Locate every blood parasite and identify its species.
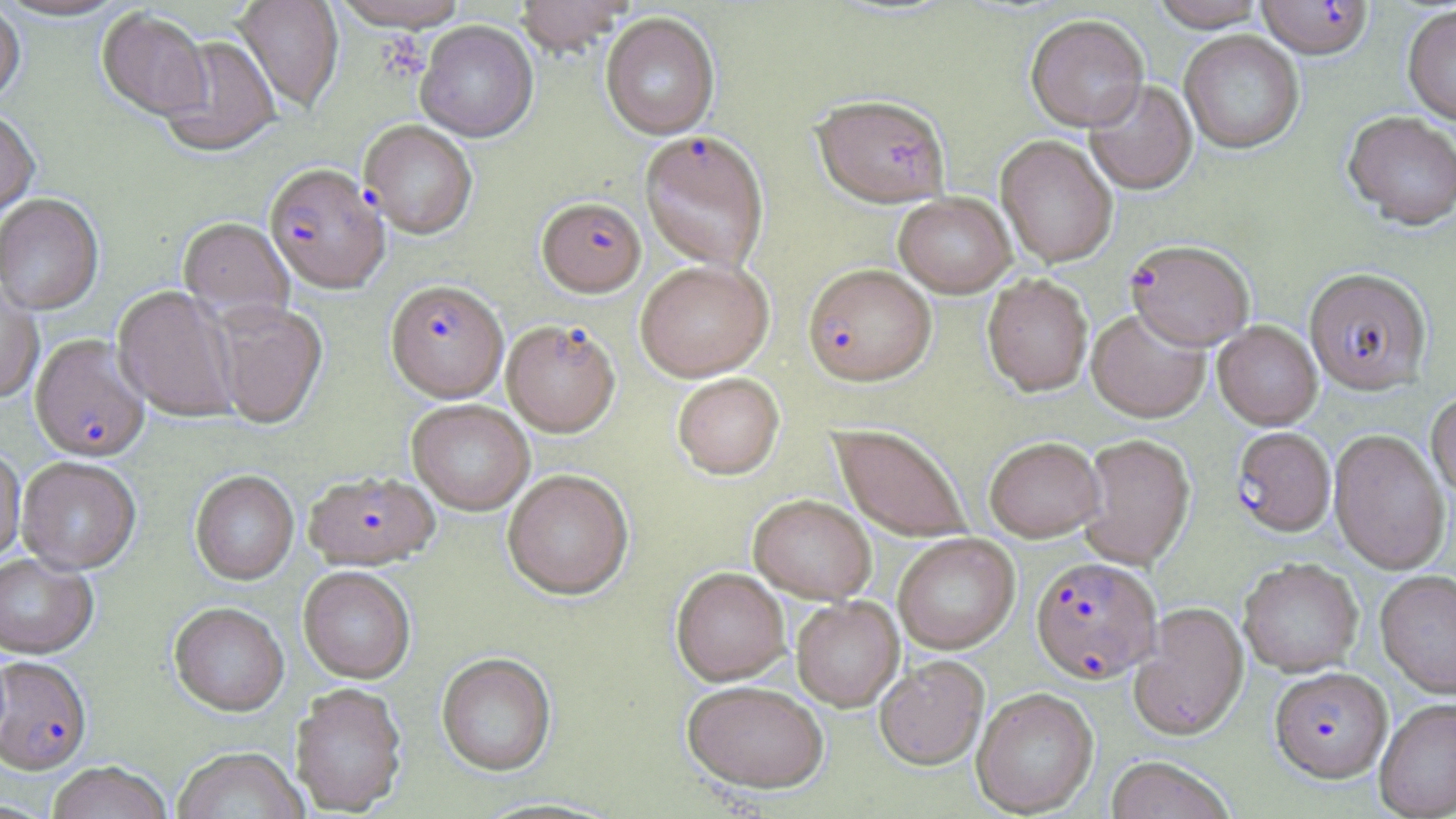

Approximate bounding boxes as named x1/y1/x2/y2 corners in pixels.
Plasmodium falciparum-infected red blood cells: (x1=1256, y1=0, x2=1374, y2=59), (x1=359, y1=121, x2=477, y2=239), (x1=639, y1=130, x2=770, y2=271), (x1=264, y1=164, x2=390, y2=295), (x1=537, y1=196, x2=646, y2=296), (x1=1126, y1=239, x2=1255, y2=350), (x1=803, y1=264, x2=936, y2=385), (x1=1305, y1=267, x2=1431, y2=394), (x1=385, y1=279, x2=508, y2=403), (x1=501, y1=319, x2=621, y2=437), (x1=30, y1=334, x2=150, y2=463), (x1=1232, y1=427, x2=1336, y2=535), (x1=305, y1=471, x2=439, y2=570), (x1=1030, y1=556, x2=1162, y2=683), (x1=0, y1=657, x2=92, y2=776), (x1=1269, y1=666, x2=1391, y2=782).
No Plasmodium ovale, Plasmodium malariae, Plasmodium vivax, Babesia divergens, or Trypanosoma brucei observed.

Summary:
  - Platelet locations: (x1=381, y1=29, x2=436, y2=82)
  - Uninfected red blood cell locations: (x1=0, y1=0, x2=127, y2=23), (x1=233, y1=0, x2=344, y2=113), (x1=329, y1=0, x2=471, y2=33), (x1=513, y1=0, x2=635, y2=55), (x1=1150, y1=0, x2=1267, y2=31), (x1=0, y1=3, x2=26, y2=108), (x1=1402, y1=4, x2=1456, y2=125), (x1=97, y1=9, x2=213, y2=122), (x1=601, y1=12, x2=720, y2=140), (x1=1025, y1=14, x2=1149, y2=131), (x1=415, y1=21, x2=539, y2=142), (x1=1179, y1=30, x2=1305, y2=153), (x1=157, y1=36, x2=281, y2=157), (x1=1084, y1=79, x2=1198, y2=195), (x1=814, y1=94, x2=950, y2=207), (x1=0, y1=111, x2=39, y2=219), (x1=1342, y1=111, x2=1456, y2=230), (x1=996, y1=135, x2=1118, y2=267), (x1=894, y1=192, x2=1016, y2=297), (x1=0, y1=195, x2=105, y2=315), (x1=178, y1=217, x2=294, y2=323), (x1=634, y1=259, x2=774, y2=382), (x1=982, y1=273, x2=1093, y2=396), (x1=0, y1=279, x2=44, y2=403), (x1=113, y1=286, x2=240, y2=423), (x1=211, y1=301, x2=327, y2=429), (x1=1087, y1=307, x2=1211, y2=422), (x1=1213, y1=321, x2=1322, y2=429), (x1=672, y1=372, x2=785, y2=479), (x1=1426, y1=389, x2=1456, y2=501), (x1=406, y1=400, x2=534, y2=516), (x1=830, y1=423, x2=972, y2=543), (x1=1328, y1=429, x2=1450, y2=573), (x1=1077, y1=433, x2=1195, y2=569), (x1=984, y1=436, x2=1104, y2=541), (x1=0, y1=446, x2=25, y2=566), (x1=16, y1=459, x2=141, y2=575), (x1=502, y1=468, x2=634, y2=601), (x1=190, y1=471, x2=298, y2=586), (x1=748, y1=494, x2=876, y2=603), (x1=893, y1=533, x2=1020, y2=654), (x1=0, y1=554, x2=98, y2=660), (x1=1238, y1=557, x2=1363, y2=676), (x1=671, y1=567, x2=791, y2=685), (x1=298, y1=568, x2=416, y2=685), (x1=1375, y1=569, x2=1456, y2=697), (x1=791, y1=597, x2=904, y2=711), (x1=1130, y1=602, x2=1249, y2=740), (x1=168, y1=603, x2=288, y2=717), (x1=436, y1=653, x2=557, y2=777), (x1=874, y1=655, x2=989, y2=769), (x1=682, y1=680, x2=829, y2=794), (x1=290, y1=684, x2=407, y2=816), (x1=971, y1=686, x2=1098, y2=816), (x1=1374, y1=699, x2=1456, y2=819), (x1=172, y1=748, x2=306, y2=819), (x1=1105, y1=756, x2=1236, y2=819), (x1=47, y1=762, x2=172, y2=819)
  - Slide-level diagnosis: Plasmodium falciparum
  - Field of view: one of a larger specimen
  - Magnification: 1000x
  - Modality: light microscopy
  - Image size: 1456×819 pixels
  - Preparation: thin blood film
  - Stain: May-Grünwald-Giemsa